Name the cell type shown.
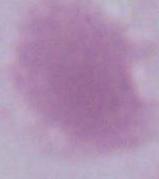

An erythrocyte.

Micrograph. Captured at 1000x magnification.